Classify this cell by malaria status.
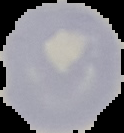
Uninfected.

preparation = thin blood smear
image type = segmented cell region with the area outside set to black
image size = 124×133 pixels